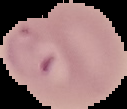

{
  "image_size": "127×109 pixels",
  "preparation": "thin blood film",
  "malaria_status": "parasitized",
  "image_type": "segmented cell region on a black background"
}